Assess this cell for malaria.
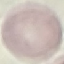

It is uninfected.

Thin blood smear. Acquired by smartphone through the microscope eyepiece. Giemsa stain. Cell patch, automatically extracted from a larger field of view and resized to 64 × 64 pixels.